Assess this cell for malaria.
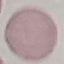

It is uninfected.

{
  "preparation": "thin blood film",
  "capture": "smartphone through the microscope eyepiece",
  "stain": "Giemsa",
  "image_type": "automatically extracted cell patch, resized to 64 × 64 pixels"
}